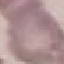

Malaria status: uninfected. Giemsa-stained preparation. Thin blood smear. Cell patch, automatically extracted from a larger field of view and resized to 64 × 64 pixels. Photographed with a smartphone camera at the microscope eyepiece.